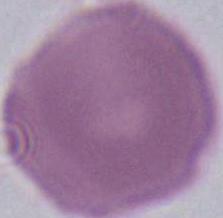 Captured at 1000x magnification. Micrograph. A red blood cell is shown.